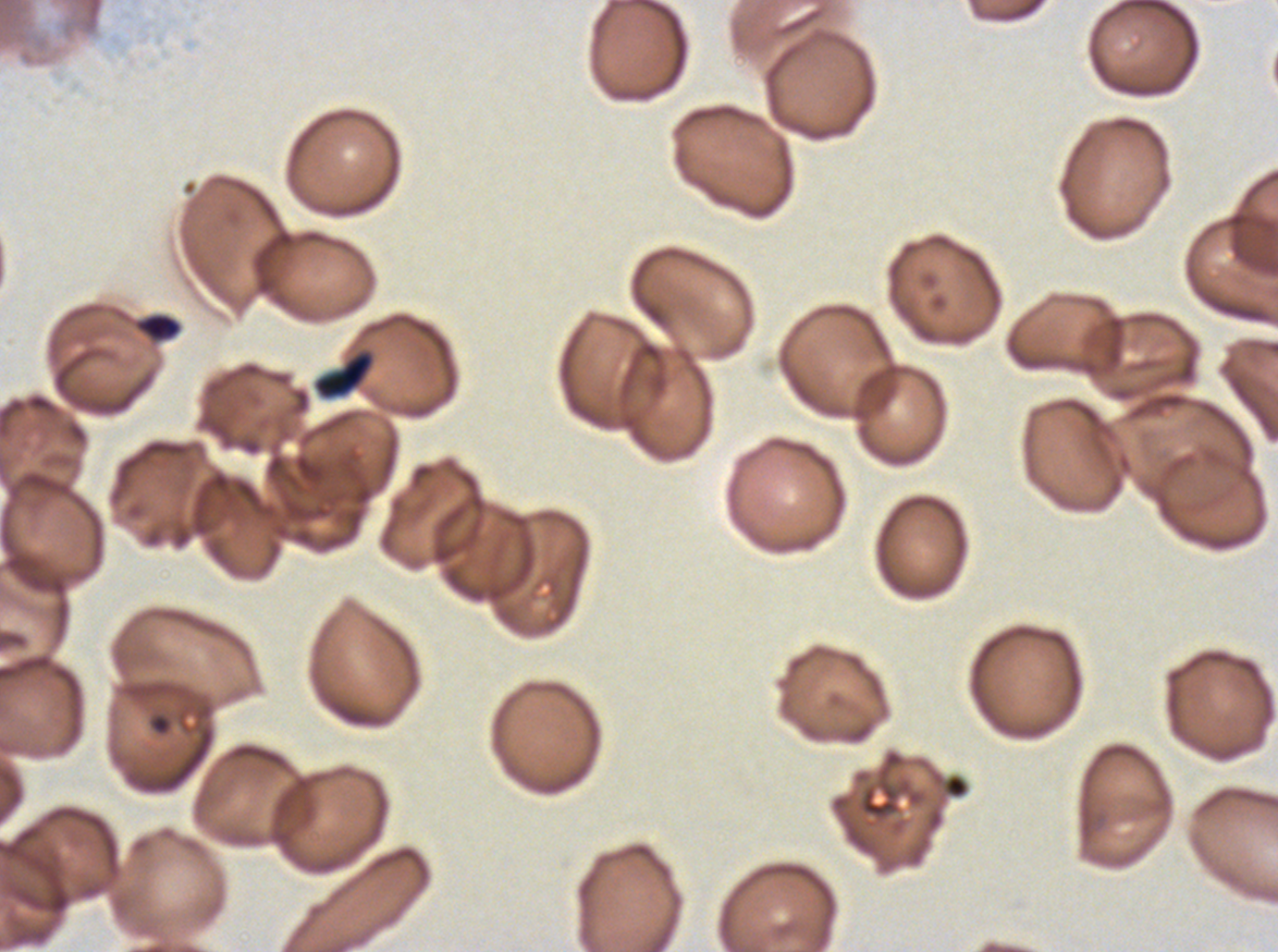

Approximate bounding rectangles given as corner coordinates in pixels from the top-left.
Summary:
  - Debris locations: (x1=133, y1=312, x2=182, y2=343), (x1=314, y1=351, x2=374, y2=399), (x1=151, y1=715, x2=170, y2=734)
  - Image size: 1278×952 pixels
  - Specimen: P. falciparum from a patient in The Gambia, cultured ex vivo for 24 to 48 hours
  - Stain: Giemsa
  - Field of view: sub-image separated from a larger composite
  - Preparation: thin blood smear